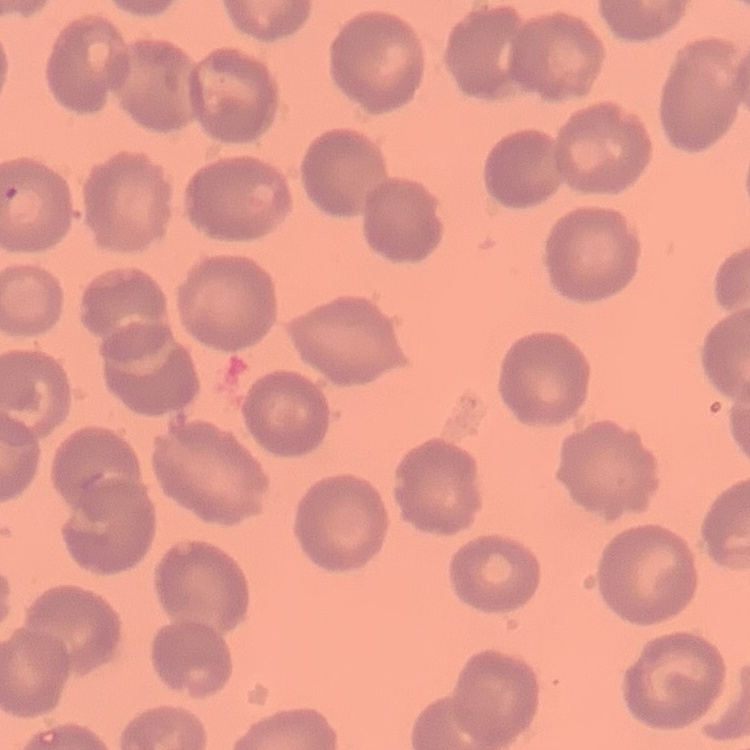
red blood cell morphology = no rouleaux formation
stain = Field's or Giemsa
preparation = thin blood smear
image type = square crop of a larger photomicrograph